Comment on the morphology of the erythrocytes.
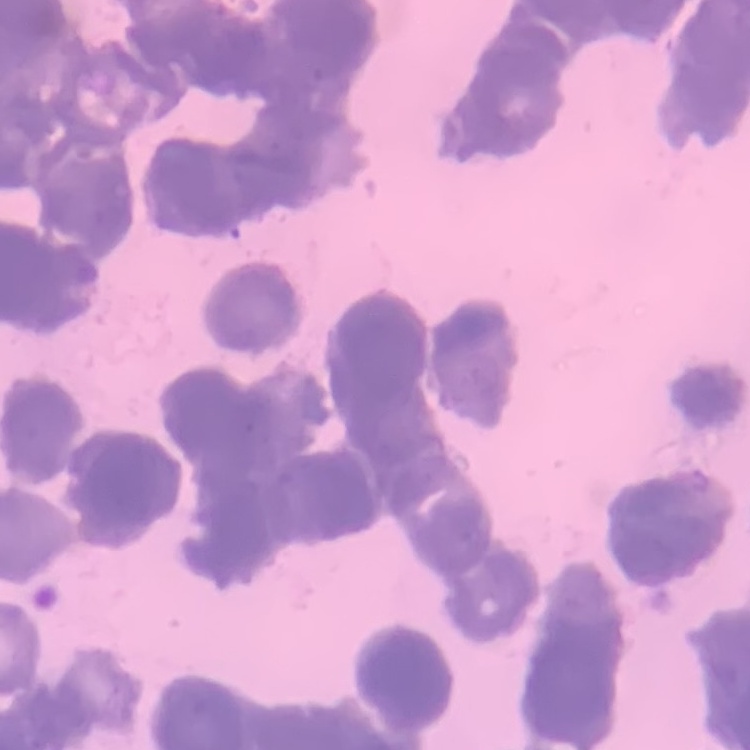
Rouleaux formation.

image_type: one tile cut from a larger photomicrograph
preparation: thin peripheral smear
stain: Field's or Giemsa